Outline each Plasmodium falciparum-infected red blood cell.
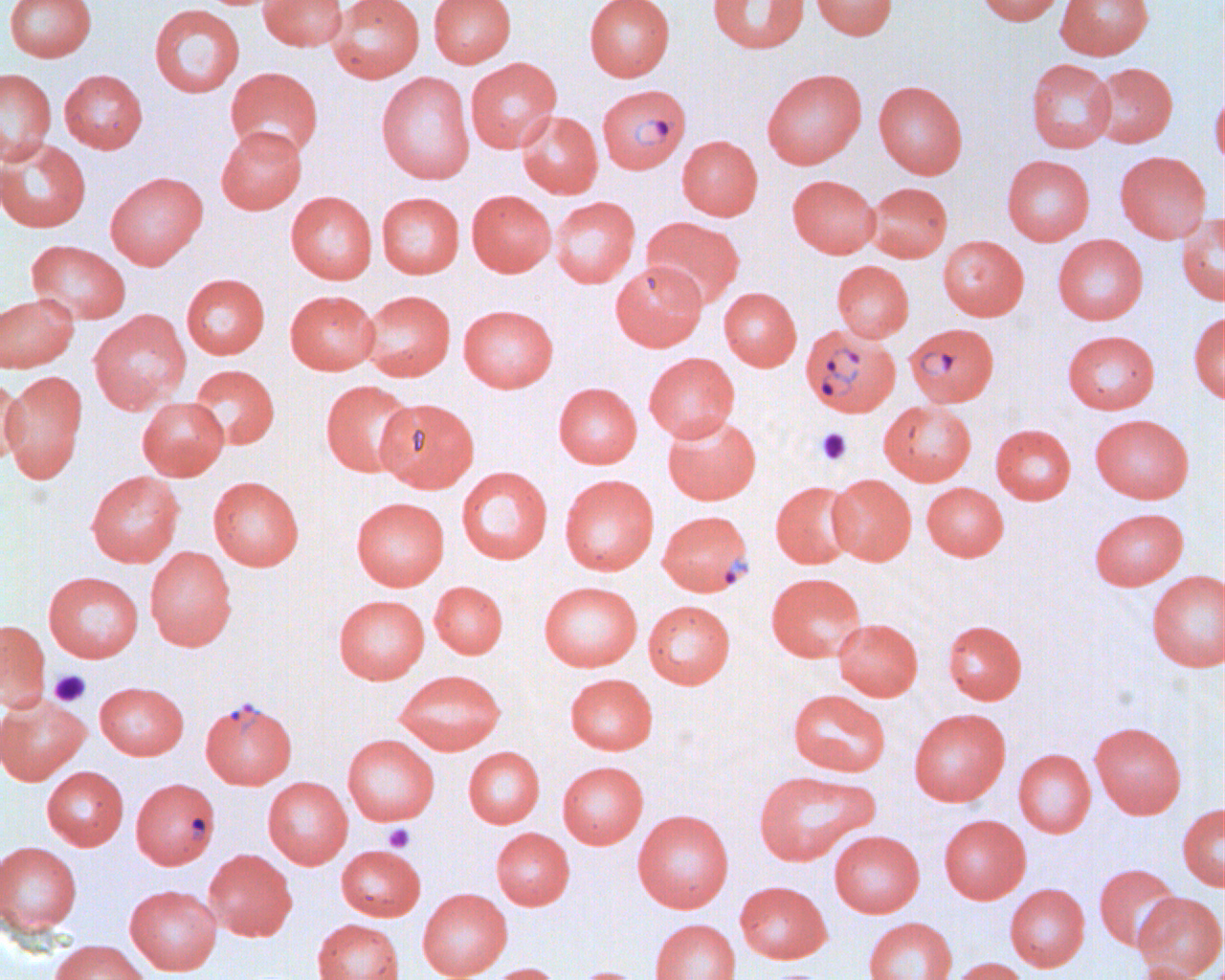

Approximate bounding boxes as (x1, y1, x2, y2) in pixels.
Plasmodium falciparum-infected red blood cells: (596, 83, 690, 174), (904, 323, 998, 408), (801, 326, 901, 420), (663, 509, 759, 595), (200, 697, 297, 789), (131, 778, 220, 868).

slide-level diagnosis = Plasmodium falciparum
platelet locations = approximate bounding boxes as (x1, y1, x2, y2) in pixels: (815, 427, 852, 466), (49, 669, 91, 707), (383, 823, 415, 852), (766, 970, 827, 980)
magnification = 1000x
image size = 1225×980 pixels
preparation = thin blood smear
uninfected red blood cell locations = approximate bounding boxes as (x1, y1, x2, y2) in pixels: (4, 0, 97, 62), (258, 0, 348, 51), (328, 0, 425, 83), (428, 0, 516, 68), (584, 0, 675, 81), (707, 0, 810, 54), (810, 0, 898, 39), (976, 0, 1066, 26), (1056, 0, 1153, 60), (149, 3, 245, 97), (465, 58, 562, 153), (1026, 58, 1116, 153), (1088, 62, 1178, 147), (225, 66, 323, 159), (0, 68, 57, 164), (762, 68, 867, 169), (59, 69, 147, 153), (376, 71, 475, 184), (873, 81, 968, 179), (1210, 88, 1223, 172), (517, 111, 603, 198), (216, 125, 306, 214), (677, 136, 763, 221), (0, 137, 91, 232), (1114, 150, 1210, 244), (1002, 154, 1095, 245), (105, 171, 208, 269), (787, 174, 880, 258), (865, 181, 952, 262), (466, 190, 556, 277), (286, 191, 377, 284), (377, 192, 464, 278), (550, 196, 640, 288), (1177, 212, 1223, 306), (641, 217, 744, 309), (1053, 235, 1148, 325), (938, 236, 1029, 321), (26, 240, 131, 325), (832, 260, 914, 342), (610, 262, 707, 350), (181, 273, 270, 359), (719, 287, 802, 371), (285, 290, 380, 374), (360, 290, 456, 381), (0, 293, 79, 373), (458, 304, 558, 392), (88, 309, 191, 414), (1188, 311, 1225, 404), (1062, 329, 1160, 414), (643, 352, 740, 442), (188, 364, 280, 450), (1, 370, 88, 483), (0, 378, 27, 466), (320, 380, 418, 477), (553, 382, 642, 468), (137, 397, 229, 480), (375, 398, 480, 492), (878, 400, 976, 486), (663, 413, 761, 505), (1090, 413, 1194, 503), (990, 424, 1076, 504), (456, 466, 553, 564), (86, 470, 185, 567), (559, 474, 659, 575), (827, 474, 916, 565), (208, 476, 304, 570), (770, 481, 860, 568), (922, 482, 1009, 561), (351, 497, 450, 590), (1089, 507, 1188, 590), (145, 546, 237, 650), (1146, 570, 1225, 671), (43, 571, 144, 662), (766, 572, 867, 662), (429, 581, 508, 658), (539, 581, 642, 671), (334, 594, 429, 683), (643, 600, 735, 688), (832, 618, 923, 700), (942, 619, 1027, 704), (0, 620, 50, 711), (394, 669, 506, 755), (565, 673, 658, 754), (94, 681, 188, 759), (787, 689, 891, 777), (0, 693, 90, 785), (909, 708, 1010, 805), (1090, 722, 1186, 818), (342, 734, 439, 825), (463, 746, 545, 828), (1014, 749, 1096, 837), (557, 761, 648, 848), (42, 766, 129, 850), (753, 769, 878, 866), (263, 776, 353, 868), (1177, 803, 1225, 891), (632, 809, 734, 912), (938, 814, 1031, 903), (491, 827, 574, 909), (829, 830, 925, 917), (0, 841, 83, 937), (336, 844, 426, 921), (204, 848, 297, 941), (1093, 864, 1183, 952), (734, 881, 832, 963), (1005, 883, 1090, 971), (125, 885, 222, 975), (417, 888, 512, 980), (1133, 892, 1225, 979), (863, 917, 957, 980), (311, 918, 405, 980), (649, 918, 741, 980), (49, 939, 150, 980), (947, 957, 1030, 980), (1132, 961, 1213, 980), (481, 963, 564, 980), (570, 966, 646, 980)
modality = light microscopy
field of view = single